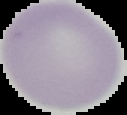 Segmented cell region on a black background. Image is 127×115 pixels. From a thin blood smear. Malaria status: uninfected.